Assess this cell for malaria.
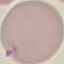
Parasitized.

Giemsa stain. Acquired by smartphone through the microscope eyepiece. Cell patch, automatically extracted from a larger field of view and resized to 64 × 64 pixels. Thin smear of blood.